Classify this cell by malaria status.
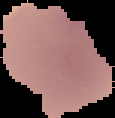

It is parasitized.

The area outside the segmented cell region is set to black. From a thin blood film. Image is 115×118 pixels.